Give the position of every Plasmodium parasite.
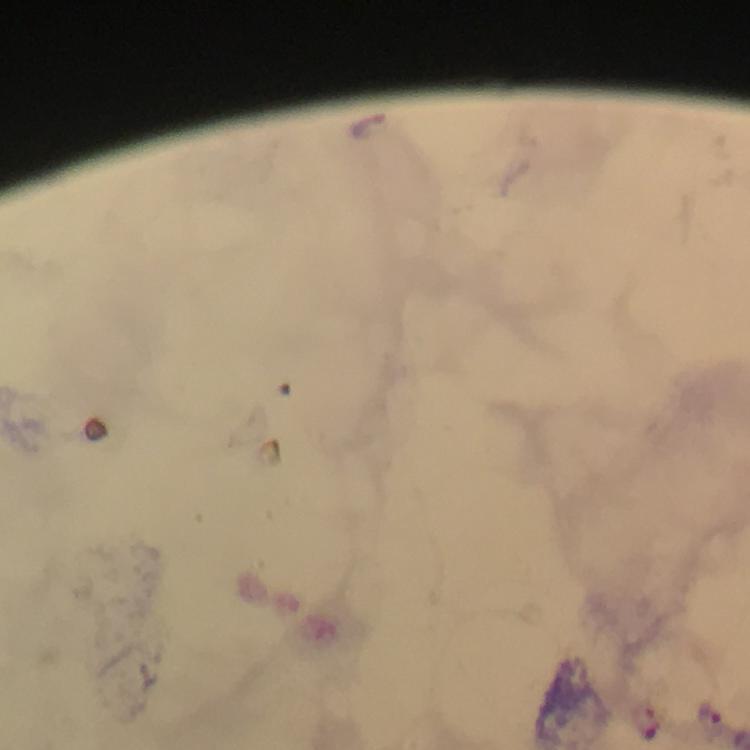

Approximate centers as {x, y} in pixels.
Plasmodium parasites: {368, 125}, {710, 715}, {647, 720}.

immersion oil = used
magnification = 100x
image size = 750×750 pixels
cropped from = a single field of view
preparation = thick blood film
context = from a diagnostic examination for malaria
stain = Giemsa
capture = smartphone photograph through a microscope